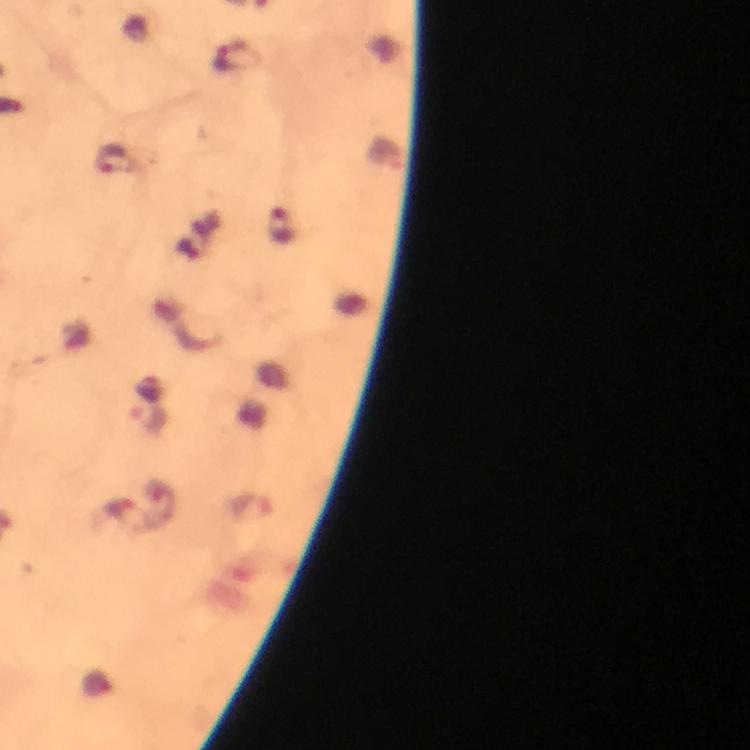
Approximate object centers, in pixels from the top-left corner.
Summary:
  - Malaria parasite locations: (x=234, y=55), (x=111, y=156), (x=281, y=227), (x=149, y=417), (x=251, y=505)
  - Stain: Giemsa
  - Magnification: 100x
  - Immersion oil: applied
  - Context: from a diagnostic examination for malaria
  - Cropped from: one field of view
  - Preparation: thick blood smear
  - Capture: smartphone photograph through a microscope
  - Image size: 750×750 pixels